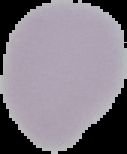

Summary:
  - Preparation: thin blood smear
  - Image size: 127×154 pixels
  - Image type: segmented cell region with the area outside set to black
  - Malaria status: uninfected